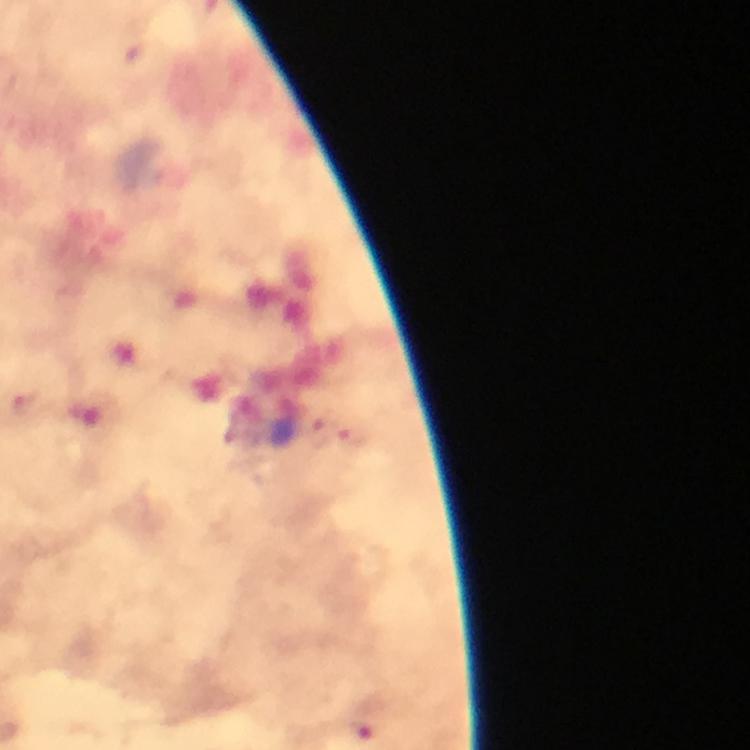
Approximate object centers, in pixels from the top-left corner.
Summary:
  - Plasmodium parasite locations: (x=319, y=431), (x=352, y=438)
  - Preparation: thick smear
  - Capture: smartphone photograph through a microscope
  - Stain: Giemsa
  - Context: from a diagnostic examination for malaria
  - Immersion oil: used
  - Magnification: 100x
  - Cropped from: a single field of view
  - Image size: 750×750 pixels